Locate every malaria parasite.
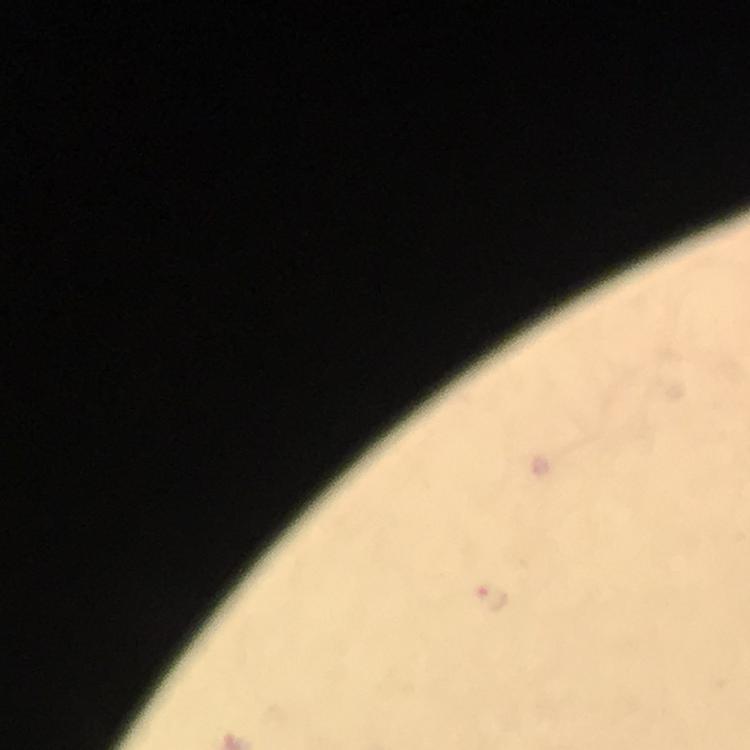

Approximate centers as {x, y} in pixels.
Malaria parasites: {490, 597}.

Thick blood smear. Photographed with a smartphone mounted on the microscope. Giemsa-stained preparation. Immersion oil applied. From a diagnostic examination for malaria. A crop from one field of view. At 100x magnification. Image is 750×750 pixels.